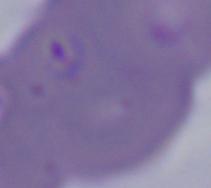 Micrograph. A Babesia parasite is shown. 1000x magnification.